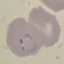

Summary:
  - Result: malaria parasites identified
  - Preparation: thin blood smear
  - Capture: smartphone through the microscope eyepiece
  - Stain: Giemsa
  - Image type: cell patch, automatically extracted from a larger field of view and resized to 64 × 64 pixels